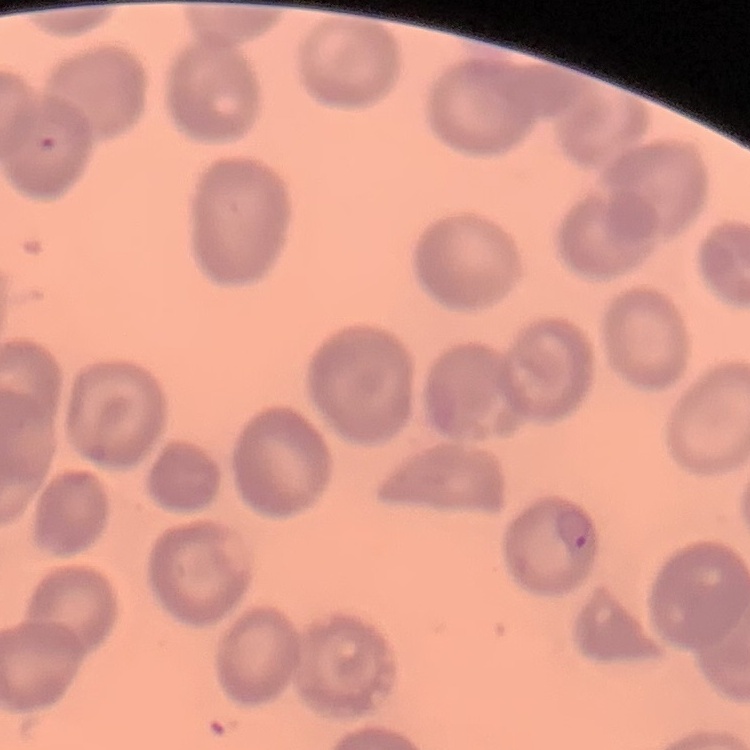

red blood cell morphology = no rouleaux formation
image type = square crop of a larger photomicrograph
stain = Field's or Giemsa
preparation = thin blood smear